Give a bounding box for every malaria parasite, every leukocyte, and every artifact (stain precipitate or debris).
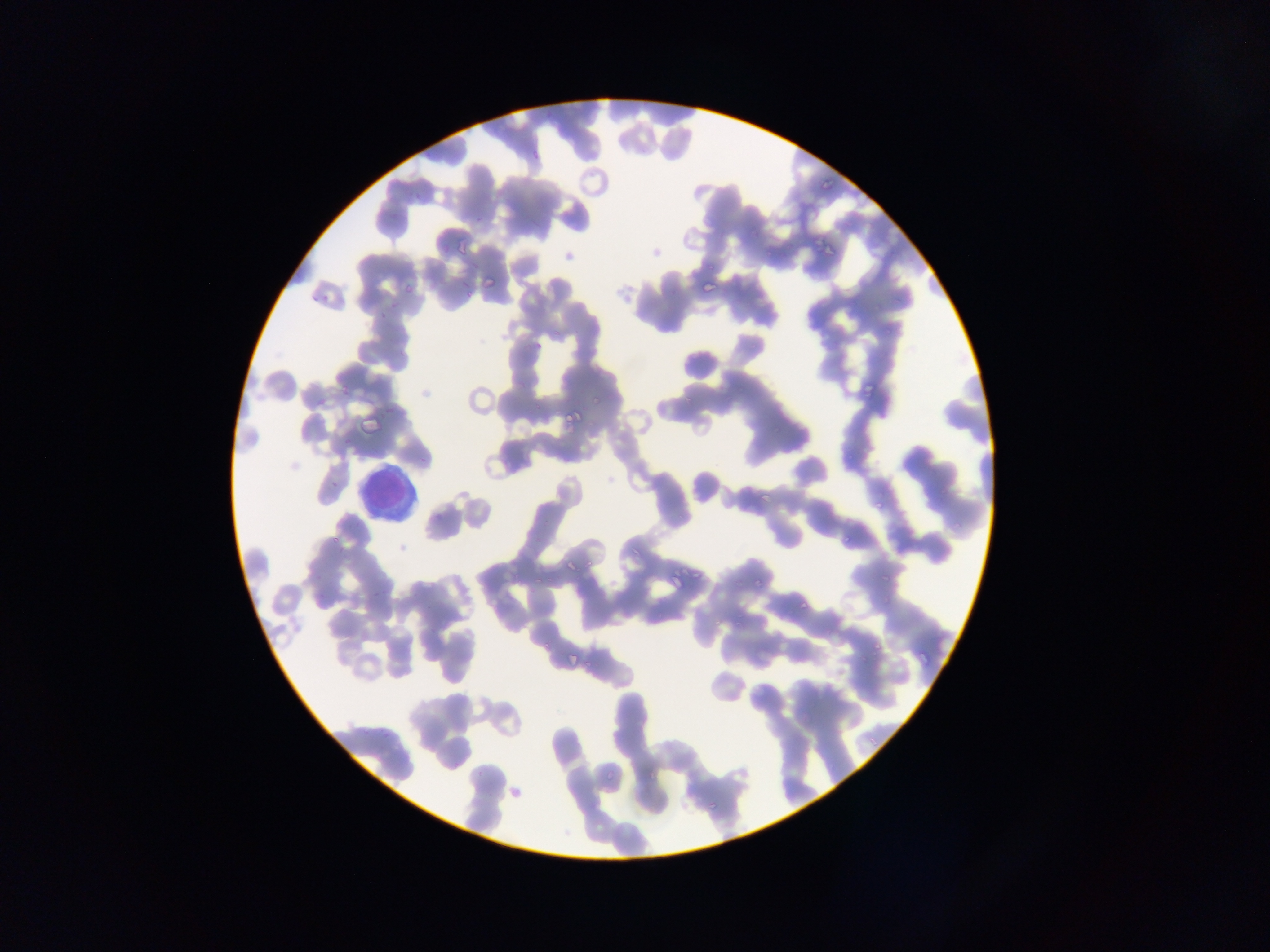

Approximate bounding boxes as (left, top, right, bottom) in pixels.
Malaria parasites: (819, 175, 836, 199), (824, 239, 838, 260), (481, 267, 504, 286), (700, 279, 717, 297), (861, 369, 880, 393), (564, 406, 585, 429), (358, 413, 382, 439), (341, 434, 355, 450), (417, 452, 433, 469), (870, 497, 892, 514), (841, 534, 850, 544), (563, 557, 581, 575), (668, 568, 695, 591), (877, 569, 891, 580), (754, 572, 768, 589), (793, 598, 804, 615), (426, 622, 441, 639), (868, 641, 880, 655), (915, 648, 932, 668), (566, 649, 587, 670), (705, 797, 720, 813).
Leukocytes: (352, 463, 418, 521).

Mobile-phone photograph taken through the microscope. Thin blood smear. Sample from Ghana. Single field of view. Image is 1270×952 pixels.